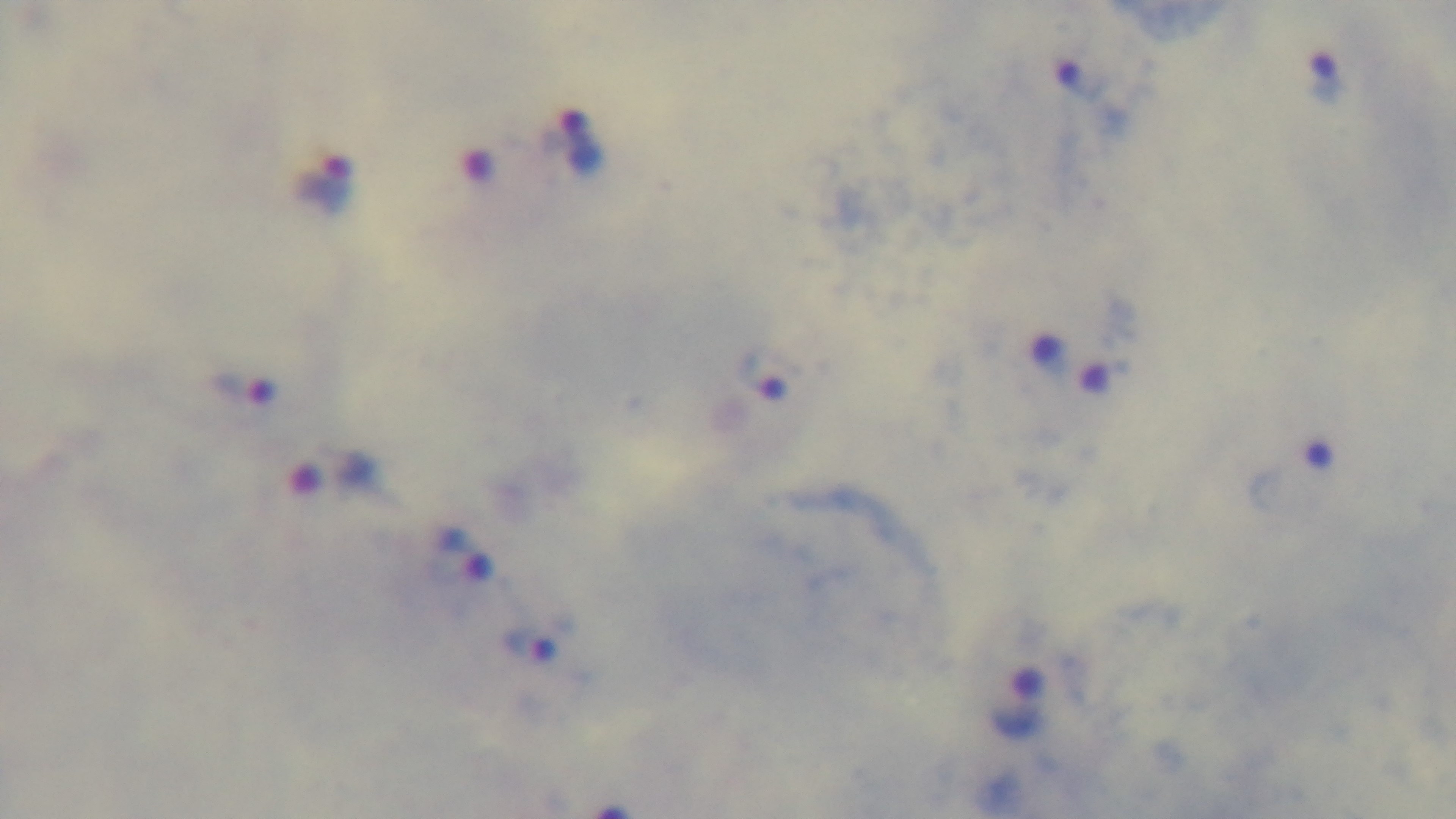

Malaria status: positive. Giemsa-stained. Oil-immersion objective, 100x. One field from the slide. Captured with a mounted 4K digital camera. Preparation: thick smear. Photomicrograph.